Locate every blood parasite and identify its species.
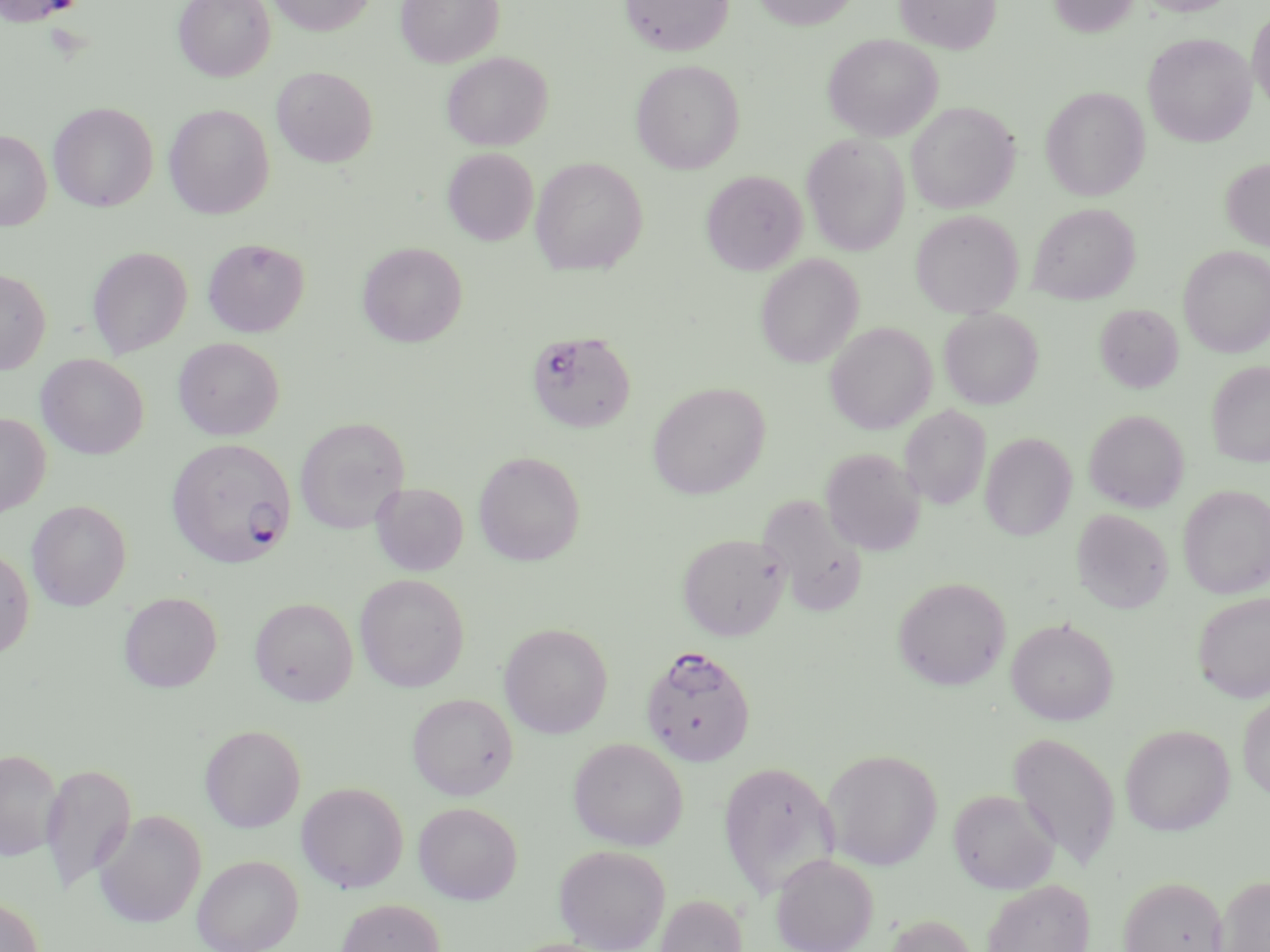
Approximate bounding boxes as (x1,y1)-(x2,y2) corner pairs in pixels.
Plasmodium falciparum-infected red blood cells: (526,330)-(636,433), (166,437)-(296,569), (640,644)-(756,766).
No Plasmodium ovale, Plasmodium malariae, Plasmodium vivax, Babesia divergens, or Trypanosoma brucei observed.

slide-level diagnosis = Plasmodium falciparum
modality = optical microscopy
stain = May-Grünwald-Giemsa
image size = 1270×952 pixels
preparation = thin blood film
field of view = single
magnification = 1000x
uninfected red blood cell locations = approximate bounding boxes as (x1,y1)-(x2,y2) corner pairs in pixels: (1,0)-(86,26), (173,0)-(275,81), (266,0)-(376,36), (395,0)-(504,67), (619,0)-(734,56), (751,0)-(860,30), (895,0)-(1000,54), (1047,0)-(1141,37), (1135,0)-(1242,16), (1248,8)-(1270,116), (1143,33)-(1257,147), (823,34)-(942,141), (441,52)-(553,150), (630,59)-(745,174), (271,66)-(378,167), (1040,87)-(1150,201), (49,102)-(158,212), (906,102)-(1020,213), (164,104)-(275,219), (0,130)-(52,230), (802,133)-(910,256), (442,148)-(539,245), (530,157)-(648,275), (1220,157)-(1270,252), (701,170)-(808,274), (1028,203)-(1140,304), (910,210)-(1023,318), (203,238)-(309,337), (357,242)-(467,347), (1179,245)-(1270,357), (87,246)-(192,357), (755,254)-(864,369), (0,267)-(51,374), (1095,303)-(1183,393), (939,308)-(1043,409), (825,322)-(937,434), (173,337)-(285,440), (36,353)-(149,459), (1206,360)-(1270,466), (648,382)-(770,499), (899,405)-(991,510), (1085,410)-(1189,513), (0,412)-(50,518), (294,417)-(409,533), (980,433)-(1077,541), (820,448)-(926,556), (474,450)-(585,566), (371,482)-(469,576), (1178,484)-(1270,598), (758,493)-(869,616), (26,500)-(131,611), (1072,509)-(1173,614), (677,532)-(790,640), (0,545)-(35,659), (355,573)-(469,692), (893,577)-(1010,690), (119,591)-(222,692), (1191,591)-(1270,703), (250,598)-(358,706), (1005,617)-(1119,725), (499,623)-(613,738), (407,693)-(519,800), (1237,694)-(1270,801), (200,724)-(305,832), (1119,724)-(1235,835), (1008,731)-(1120,869), (568,737)-(688,850), (822,748)-(943,870), (1,749)-(64,861), (717,760)-(839,901), (40,762)-(136,893), (296,781)-(409,893), (948,788)-(1059,894), (413,801)-(522,904), (93,810)-(206,928), (554,845)-(671,951), (771,853)-(878,952), (192,854)-(304,952), (1118,875)-(1228,952), (1212,875)-(1270,952), (982,879)-(1094,952), (0,894)-(45,952), (655,894)-(748,952), (336,899)-(445,952), (880,914)-(980,952)